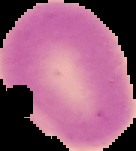

Cell region segmented out of the field of view; the surrounding area is masked to black. Result: no Plasmodium parasites detected. Image is 136×151 pixels. From a thin blood film.